Comment on the morphology of the red blood cells.
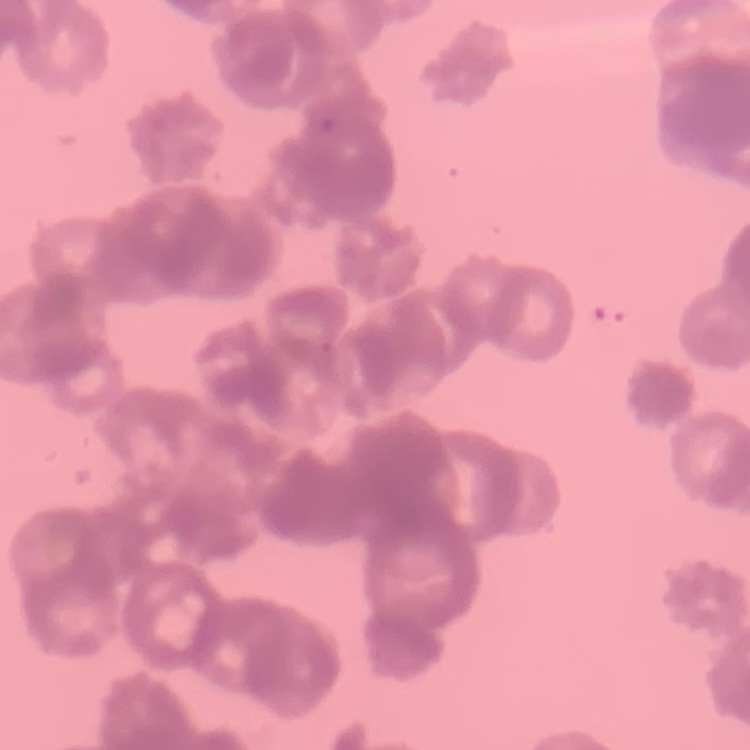
They show rouleaux formation.

Square crop of a larger photomicrograph. Thin blood film. Field's or Giemsa stain.